Locate every blood parasite and identify its species.
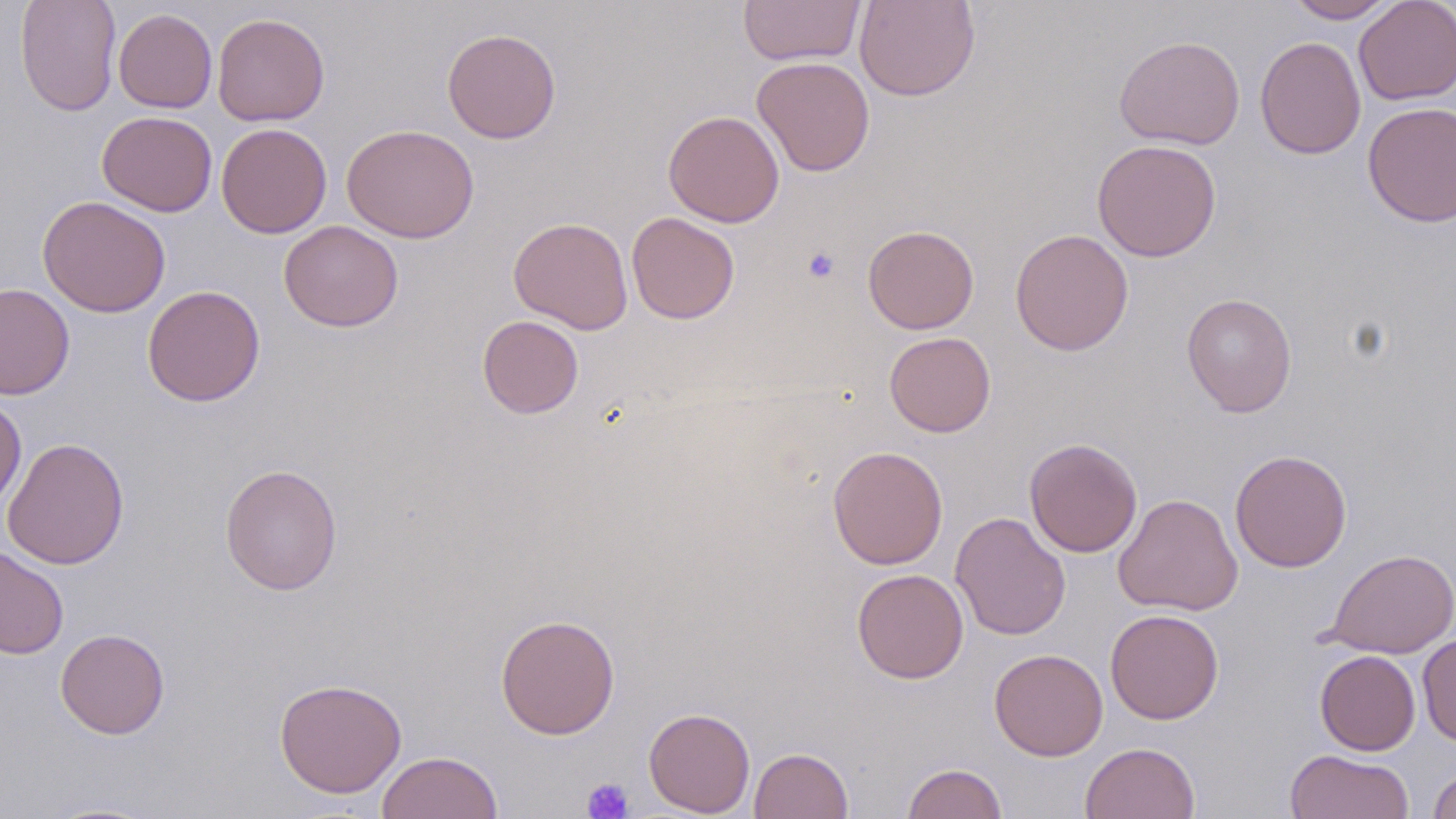

No blood parasites observed.

Approximate bounding boxes as (x1, y1, x2, y2) in pixels. Uninfected red blood cell locations: (15, 0, 121, 116), (738, 0, 865, 66), (853, 0, 980, 101), (1284, 0, 1399, 23), (1354, 0, 1456, 105), (114, 8, 217, 113), (212, 12, 330, 126), (441, 27, 562, 144), (1114, 35, 1245, 150), (1254, 36, 1366, 160), (752, 57, 875, 176), (1362, 101, 1456, 228), (96, 110, 217, 217), (663, 110, 784, 227), (216, 122, 332, 238), (341, 123, 480, 243), (1092, 139, 1222, 262), (37, 195, 171, 317), (626, 212, 740, 324), (508, 216, 633, 334), (279, 220, 404, 332), (863, 225, 979, 334), (1010, 228, 1134, 356), (0, 283, 75, 400), (142, 285, 266, 406), (1181, 293, 1297, 417), (477, 315, 584, 419), (884, 331, 996, 436), (0, 396, 26, 514), (2, 437, 130, 569), (1024, 438, 1143, 558), (827, 446, 948, 569), (1229, 449, 1352, 572), (219, 463, 343, 595), (1113, 493, 1243, 616), (950, 511, 1070, 640), (0, 544, 69, 659), (1325, 548, 1456, 659), (851, 568, 969, 684), (1104, 608, 1224, 724), (495, 613, 620, 739), (55, 628, 170, 738), (1417, 633, 1456, 746), (989, 648, 1108, 761), (1315, 650, 1420, 755), (274, 678, 407, 798), (643, 707, 756, 817), (1080, 742, 1200, 819), (749, 747, 853, 819), (1284, 749, 1414, 819), (376, 751, 503, 819), (901, 762, 1008, 819), (1428, 766, 1456, 819), (37, 800, 168, 818). Platelet locations: (802, 247, 840, 284), (582, 777, 634, 818). Slide-level diagnosis: negative for blood parasites. Light microscopy. Thin blood film. Captured at 1000x magnification. Image is 1456×819 pixels. Single field of view. May-Grünwald-Giemsa-stained preparation.